Classify this cell by malaria status.
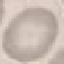

Uninfected.

capture: smartphone through the microscope eyepiece
stain: Giemsa
preparation: thin smear
image_type: cell patch, automatically extracted from a larger field of view and resized to 64 × 64 pixels